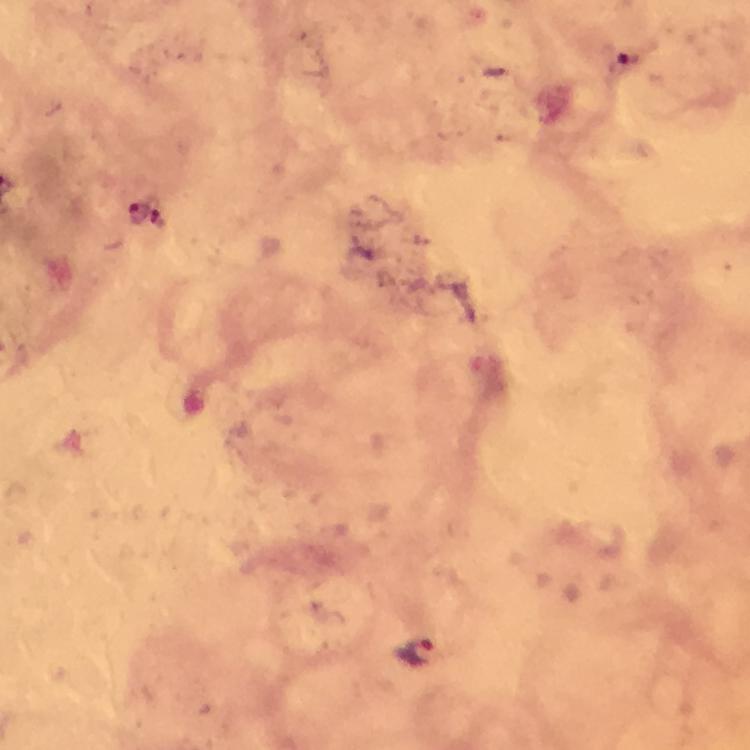
Approximate centers as (x, y) in pixels.
Summary:
  - Malaria parasite locations: (628, 57), (140, 211), (421, 654)
  - Capture: smartphone camera through the microscope
  - Magnification: 100x
  - Preparation: thick blood smear
  - Immersion oil: used
  - Cropped from: a single field of view
  - Stain: Giemsa
  - Image size: 750×750 pixels
  - Context: from a malaria diagnostic workup